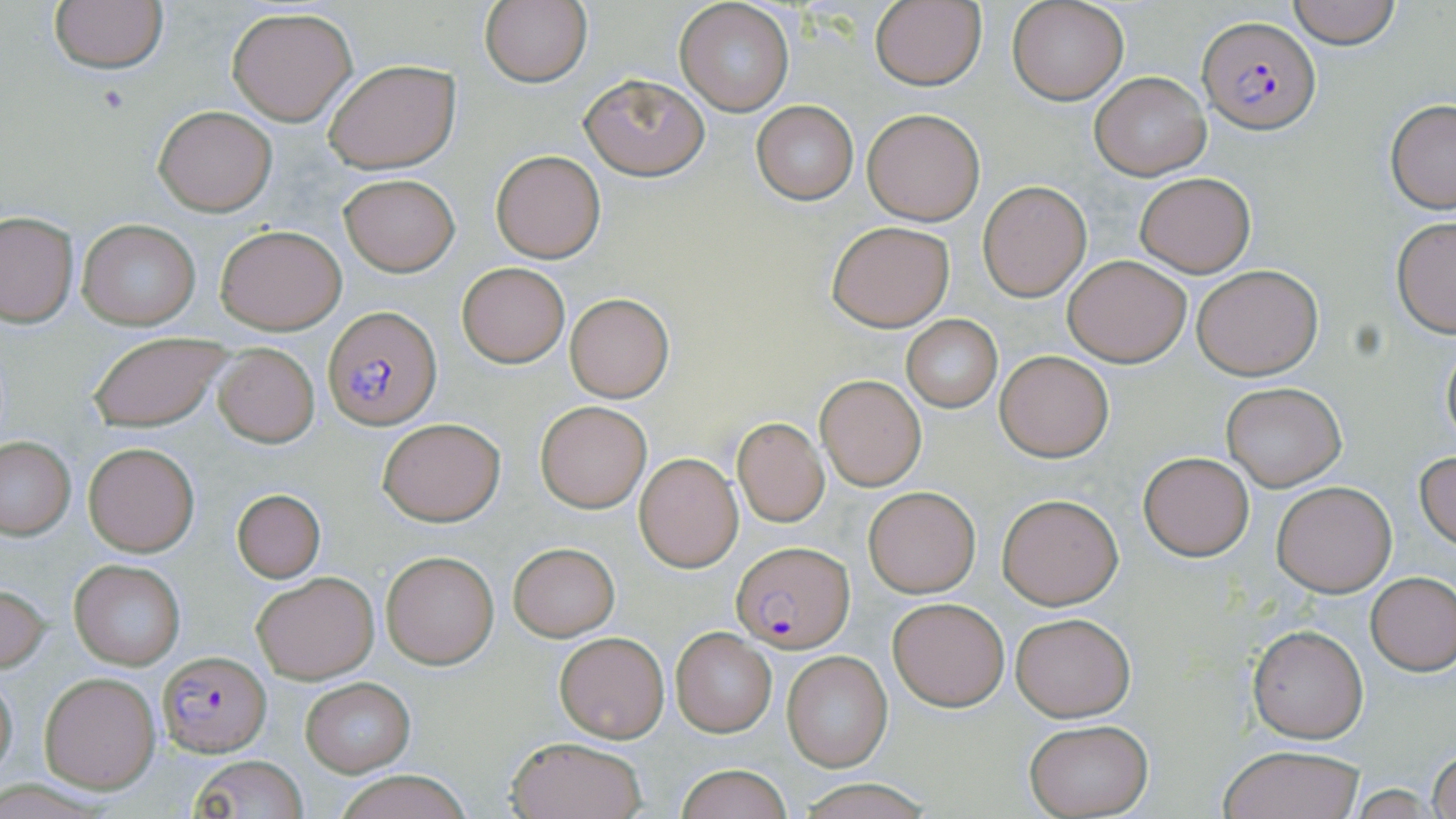 Approximate bounding boxes as (x1,y1)-(x2,y2) corner pairs in pixels. Plasmodium falciparum-infected red blood cell locations: (1197,16)-(1320,133), (323,306)-(440,429), (733,542)-(855,651), (158,652)-(272,757). Uninfected red blood cell locations: (479,0)-(594,88), (1008,0)-(1127,105), (1287,0)-(1401,48), (49,1)-(169,73), (674,1)-(795,116), (868,1)-(986,89), (227,7)-(357,126), (324,59)-(460,172), (1089,71)-(1210,181), (579,74)-(709,181), (751,100)-(858,204), (1385,100)-(1456,214), (154,104)-(277,216), (861,107)-(985,225), (491,149)-(605,263), (1133,171)-(1256,276), (339,173)-(460,276), (978,181)-(1091,301), (0,210)-(78,326), (1390,216)-(1456,338), (78,218)-(202,332), (827,220)-(955,331), (213,224)-(345,334), (1063,254)-(1193,367), (456,262)-(570,367), (1193,265)-(1323,379), (565,292)-(675,403), (901,315)-(1001,413), (88,332)-(234,433), (1440,334)-(1455,451), (213,345)-(319,446), (997,351)-(1114,462), (815,375)-(927,490), (1219,381)-(1346,491), (534,399)-(652,514), (377,416)-(506,527), (733,417)-(828,526), (1,437)-(76,539), (84,443)-(197,555), (1416,449)-(1456,552), (1139,452)-(1254,562), (635,453)-(743,571), (1272,481)-(1396,597), (863,486)-(979,597), (231,489)-(325,582), (997,493)-(1123,609), (508,543)-(619,639), (381,551)-(499,668), (69,560)-(186,669), (252,571)-(380,683), (1366,572)-(1456,674), (0,582)-(51,672), (888,597)-(1010,711), (1011,612)-(1135,720), (1249,625)-(1367,743), (671,628)-(777,737), (554,631)-(669,742), (782,651)-(892,772), (0,663)-(19,782), (39,672)-(161,792), (299,676)-(417,776), (1023,719)-(1151,818), (505,734)-(647,819), (1218,745)-(1366,819), (1430,749)-(1456,819), (188,756)-(311,818), (674,765)-(793,819), (334,769)-(473,819), (793,777)-(932,818). Platelet locations: (94,84)-(131,113). Slide-level diagnosis: Plasmodium falciparum. Image is 1456×819 pixels. May-Grünwald-Giemsa stain. Captured at 1000x magnification. Single field of view. Thin blood film. Light microscopy.